Rate the background quality.
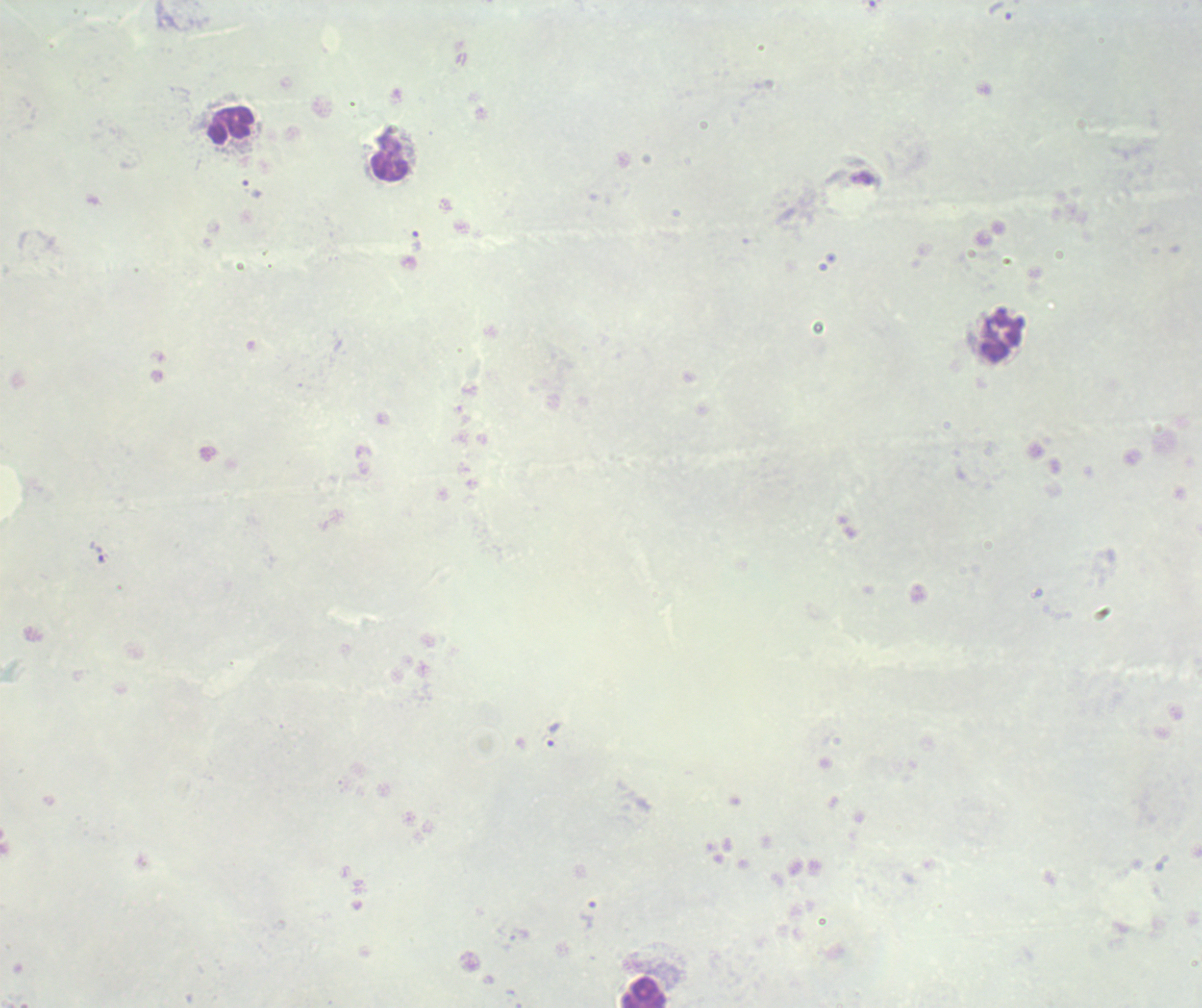

Poor.

Approximate centers as {x, y} in pixels. Trophozoite locations: {1001, 10}, {253, 189}, {416, 240}, {1002, 338}, {99, 553}, {554, 734}, {587, 914}. Leukocyte locations: {231, 125}, {390, 156}, {644, 993}. Thick blood smear. Coloration quality: bad. Single field of view. Romanowsky-stained preparation. Captured at 100x magnification. Image is 1202×1008 pixels. Result: Plasmodium parasites detected. Previously used in a real diagnosis.